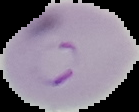
{
  "image_size": "139×112 pixels",
  "preparation": "thin blood film",
  "malaria_status": "parasitized",
  "image_type": "segmented cell region with the area outside set to black"
}